Comment on the morphology of the red blood cells.
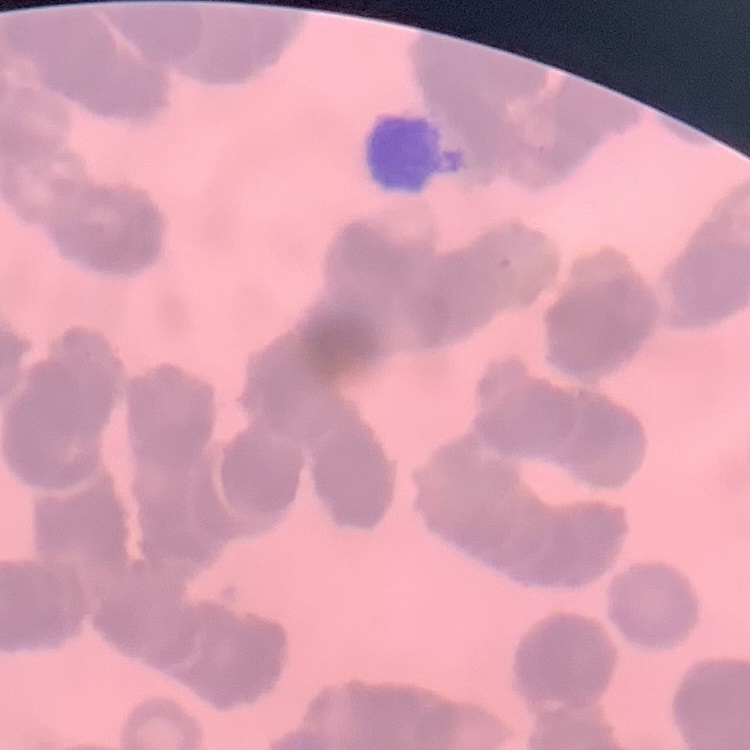
Rouleaux formation.

preparation = thin blood smear
stain = Field's or Giemsa
image type = square crop of a larger photomicrograph